Report the malaria status of this cell.
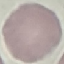
It is uninfected.

Summary:
  - Preparation: thin smear
  - Image type: cell patch, automatically extracted from a larger field of view and resized to 64 × 64 pixels
  - Stain: Giemsa
  - Capture: smartphone camera at the microscope eyepiece